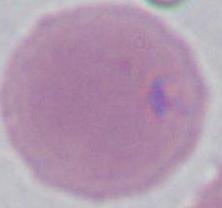

Summary:
  - Magnification: 1000x
  - Modality: micrograph
  - Identification: erythrocyte